Mark where platelets are.
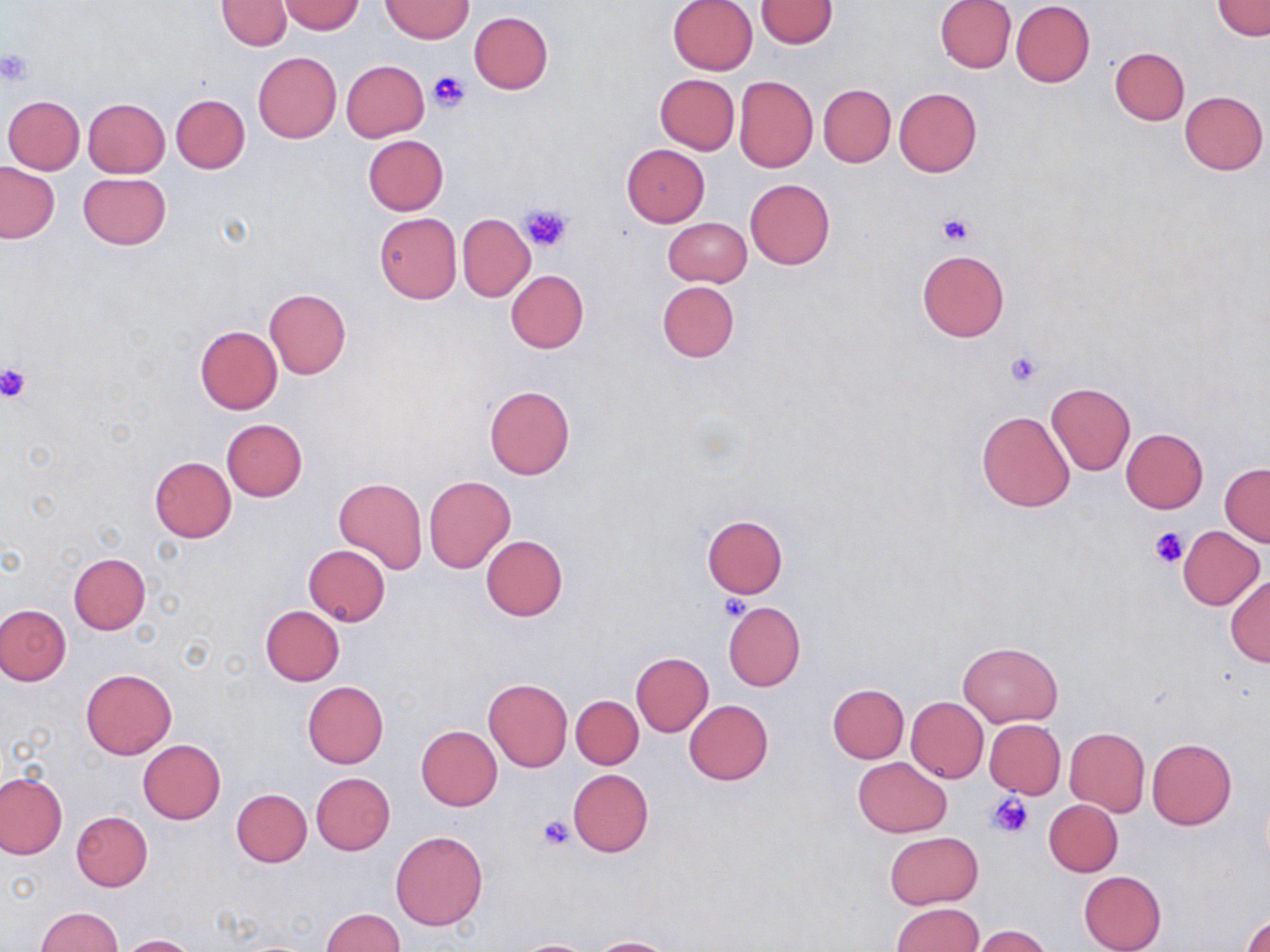
Approximate bounding boxes as (x1, y1, x2, y2) in pixels.
Platelets: (0, 49, 36, 86), (428, 71, 468, 111), (519, 203, 573, 253), (937, 214, 973, 245), (1004, 351, 1041, 387), (0, 363, 31, 403), (1150, 527, 1191, 569), (718, 593, 752, 622), (988, 793, 1033, 838), (536, 815, 575, 850).

Uninfected red blood cell locations: (216, 0, 293, 50), (667, 0, 758, 75), (755, 0, 838, 47), (935, 0, 1016, 72), (1214, 0, 1269, 40), (278, 1, 364, 34), (381, 1, 472, 43), (1011, 1, 1095, 86), (470, 12, 553, 93), (1110, 47, 1189, 125), (252, 52, 342, 143), (341, 60, 429, 141), (655, 74, 739, 154), (734, 76, 818, 172), (819, 85, 896, 168), (893, 87, 983, 177), (1180, 90, 1268, 175), (171, 94, 250, 173), (3, 96, 84, 175), (83, 98, 170, 178), (363, 135, 448, 215), (621, 144, 710, 227), (0, 163, 59, 243), (78, 172, 170, 250), (745, 179, 836, 270), (668, 197, 835, 276), (374, 211, 462, 304), (458, 213, 534, 301), (663, 216, 751, 286), (917, 249, 1009, 342), (505, 270, 589, 353), (656, 281, 739, 362), (263, 287, 351, 379), (194, 326, 283, 414), (1045, 382, 1135, 476), (484, 384, 575, 480), (976, 410, 1074, 513), (222, 419, 307, 502), (1120, 428, 1208, 513), (149, 457, 237, 542), (1221, 463, 1270, 546), (424, 475, 516, 574), (334, 477, 427, 574), (702, 515, 788, 597), (1178, 526, 1265, 610), (480, 535, 568, 621), (304, 545, 391, 625), (68, 553, 150, 634), (1226, 575, 1270, 667), (722, 602, 805, 691), (1, 604, 71, 685), (260, 606, 345, 686), (959, 642, 1062, 726), (630, 652, 713, 736), (81, 668, 176, 758), (483, 679, 573, 773), (302, 681, 388, 769), (827, 684, 908, 763), (571, 696, 643, 769), (906, 697, 988, 782), (685, 700, 773, 785), (984, 719, 1065, 798), (416, 725, 502, 811), (1064, 727, 1150, 817), (1146, 738, 1238, 830), (137, 739, 226, 824), (853, 757, 952, 837), (567, 769, 654, 856), (0, 772, 67, 859), (311, 773, 395, 855), (233, 788, 311, 867), (1044, 799, 1122, 876), (71, 811, 153, 891), (390, 830, 488, 931), (884, 832, 983, 908), (1078, 870, 1166, 952), (890, 903, 983, 952), (35, 906, 123, 952), (321, 908, 404, 951), (1241, 912, 1270, 952), (968, 925, 1053, 952), (118, 934, 196, 952), (588, 937, 677, 951), (512, 939, 599, 952). Slide-level diagnosis: no evidence of blood parasites. Single field of view. Captured at 1000x magnification. Optical microscopy. Image is 1270×952 pixels. May-Grünwald-Giemsa-stained preparation. Thin blood film.